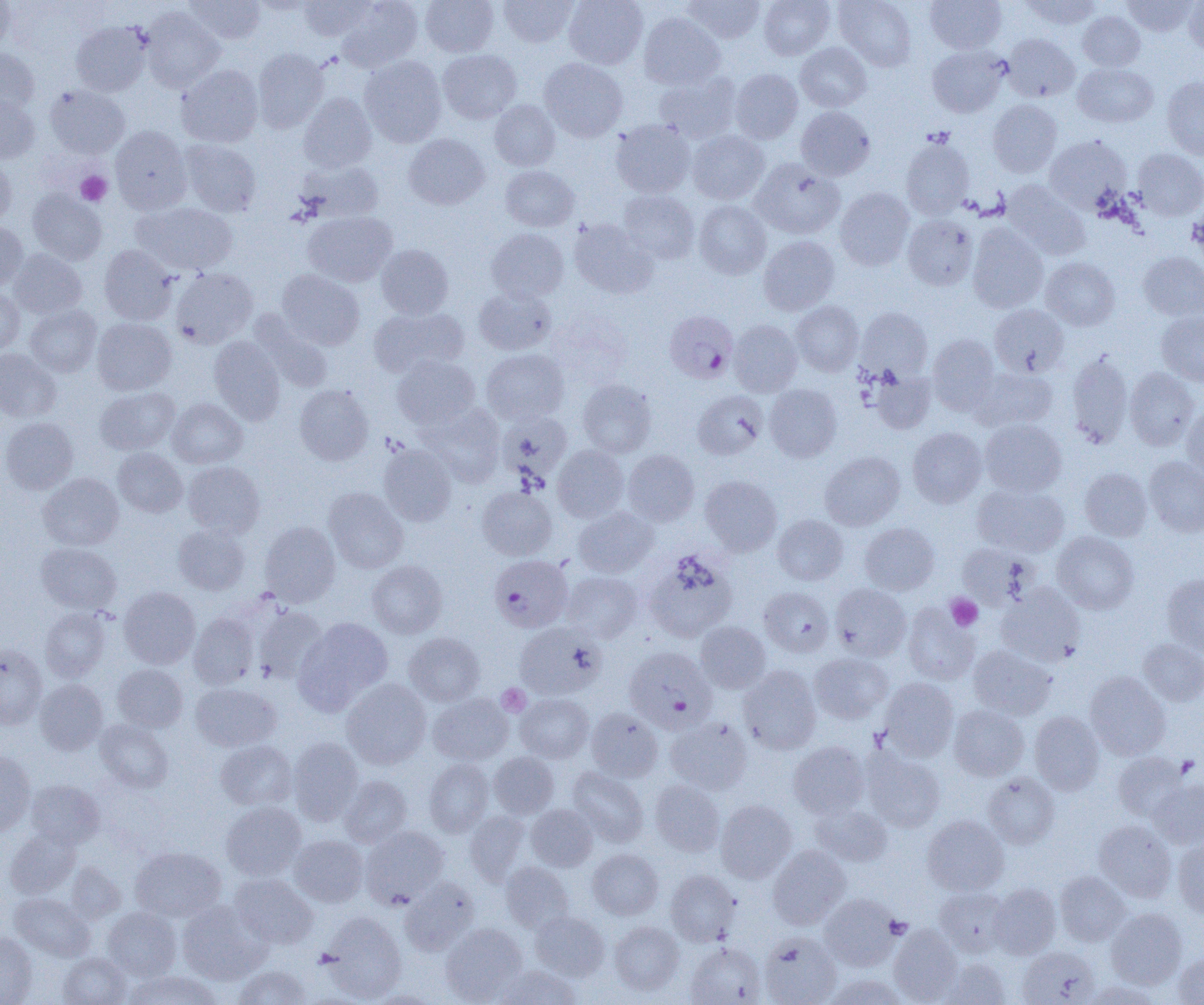
Summary:
  - Coordinate format: approximate bounding boxes as (x1, y1, x2, y2) in pixels
  - Uninfected red blood cell locations: (0, 0, 15, 54), (184, 0, 265, 45), (298, 0, 375, 40), (336, 0, 423, 72), (420, 0, 498, 57), (499, 0, 577, 47), (563, 0, 648, 69), (683, 0, 765, 45), (759, 0, 834, 60), (835, 0, 916, 71), (926, 0, 1006, 54), (1019, 0, 1102, 30), (1121, 0, 1199, 37), (1183, 0, 1204, 55), (142, 8, 225, 92), (1078, 11, 1145, 71), (639, 12, 725, 90), (71, 21, 151, 95), (1002, 34, 1079, 102), (794, 43, 872, 112), (927, 46, 1008, 117), (0, 48, 39, 113), (253, 48, 329, 134), (438, 49, 521, 124), (359, 56, 446, 147), (540, 58, 628, 142), (1072, 62, 1158, 128), (176, 65, 263, 147), (730, 68, 803, 144), (654, 72, 741, 144), (1161, 76, 1204, 159), (45, 84, 129, 158), (298, 92, 377, 172), (0, 94, 39, 163), (988, 99, 1062, 177), (489, 100, 560, 171), (795, 106, 875, 181), (610, 119, 695, 198), (109, 126, 192, 214), (688, 130, 769, 205), (404, 134, 490, 210), (1044, 135, 1131, 211), (901, 136, 974, 218), (179, 139, 261, 216), (1133, 149, 1204, 220), (0, 156, 16, 226), (750, 159, 845, 239), (297, 160, 384, 222), (500, 165, 580, 231), (1003, 181, 1090, 260), (835, 188, 914, 270), (27, 189, 107, 265), (619, 190, 699, 263), (693, 200, 771, 279), (132, 202, 237, 275), (303, 211, 397, 287), (902, 214, 978, 290), (568, 219, 658, 299), (0, 222, 28, 290), (967, 224, 1048, 313), (486, 228, 569, 302), (759, 235, 839, 315), (376, 244, 453, 319), (100, 245, 179, 325), (8, 249, 87, 319), (1138, 252, 1204, 322), (1041, 257, 1120, 330), (171, 268, 258, 349), (276, 269, 364, 350), (474, 286, 556, 355), (0, 287, 24, 355), (790, 301, 863, 376), (25, 304, 102, 377), (989, 304, 1069, 377), (369, 306, 469, 378), (855, 307, 933, 380), (251, 312, 333, 393), (1157, 312, 1204, 386), (92, 318, 176, 395), (728, 320, 802, 397), (927, 333, 999, 415), (209, 336, 285, 425), (0, 348, 61, 422), (481, 349, 569, 424), (1065, 350, 1133, 449), (392, 355, 480, 429), (971, 367, 1058, 431), (1125, 367, 1200, 451), (870, 369, 936, 434), (577, 379, 657, 458), (765, 384, 842, 462), (294, 385, 374, 466), (95, 387, 180, 455), (693, 391, 768, 460), (168, 398, 247, 468), (420, 403, 505, 487), (1182, 403, 1204, 481), (498, 412, 573, 485), (0, 417, 78, 494), (979, 419, 1066, 497), (907, 427, 987, 508), (378, 443, 457, 526), (552, 445, 629, 522), (113, 448, 187, 517), (623, 450, 699, 526), (820, 452, 905, 530), (1144, 455, 1204, 537), (183, 461, 265, 538), (1079, 467, 1152, 541), (39, 473, 124, 550), (700, 475, 782, 556), (972, 482, 1069, 556), (477, 486, 557, 560), (323, 487, 408, 573), (573, 506, 658, 577), (772, 514, 848, 585), (259, 521, 340, 607), (860, 522, 939, 595), (173, 524, 250, 595), (1052, 531, 1139, 614), (36, 542, 122, 614), (956, 542, 1035, 610), (645, 549, 737, 642), (367, 560, 447, 638), (562, 571, 642, 643), (1161, 573, 1204, 655), (831, 584, 911, 661), (996, 584, 1086, 667), (119, 587, 200, 669), (759, 587, 834, 657), (902, 602, 980, 685), (253, 605, 327, 683), (40, 607, 111, 682), (188, 614, 258, 689), (295, 617, 393, 713), (695, 621, 770, 693), (514, 622, 605, 699), (404, 632, 485, 706), (1138, 638, 1204, 706), (0, 643, 47, 728), (968, 645, 1057, 720), (809, 652, 892, 724), (113, 664, 188, 732), (739, 665, 822, 755), (1085, 671, 1171, 760), (341, 678, 431, 769), (878, 678, 959, 761), (35, 679, 108, 754), (191, 682, 281, 751), (428, 693, 512, 765), (515, 693, 594, 762), (948, 705, 1029, 780), (586, 707, 663, 781), (1029, 711, 1105, 794), (665, 717, 753, 795), (95, 720, 173, 793), (288, 737, 363, 824), (215, 739, 297, 811), (788, 741, 869, 818), (861, 747, 945, 832), (0, 751, 36, 836), (1112, 751, 1189, 821), (489, 752, 559, 818), (424, 758, 494, 837), (567, 767, 648, 847), (983, 772, 1059, 848), (339, 775, 412, 847), (1149, 779, 1204, 849), (26, 780, 104, 849), (649, 780, 725, 856), (716, 800, 797, 883), (221, 802, 306, 880), (810, 802, 893, 867), (526, 804, 598, 871), (464, 811, 531, 886), (922, 814, 1009, 896), (1094, 819, 1176, 902), (360, 826, 448, 908), (4, 828, 80, 899), (289, 835, 368, 907), (1172, 840, 1204, 918), (768, 845, 851, 929), (131, 846, 226, 923), (587, 849, 663, 920), (500, 861, 574, 932), (65, 863, 125, 924), (665, 870, 741, 946), (1055, 871, 1131, 946), (230, 873, 318, 949), (400, 877, 479, 955), (989, 883, 1061, 959), (935, 887, 1010, 957), (10, 893, 95, 961), (819, 893, 902, 970), (177, 900, 268, 984), (102, 907, 181, 980), (1106, 908, 1187, 989), (530, 910, 610, 981), (320, 913, 406, 1002), (609, 921, 684, 995), (441, 923, 527, 1003), (889, 925, 963, 1004), (0, 932, 38, 1004), (759, 932, 841, 1005), (686, 941, 765, 1004), (1018, 945, 1100, 1004), (1172, 952, 1204, 1004), (58, 953, 132, 1004), (939, 958, 1011, 1004), (232, 965, 312, 1005), (494, 965, 581, 1004), (125, 971, 222, 1005), (824, 974, 908, 1005), (1082, 981, 1163, 1005), (366, 991, 443, 1004)
  - Plasmodium falciparum-infected red blood cell locations: (664, 310, 738, 383), (489, 554, 573, 632), (625, 645, 717, 734)
  - Platelet locations: (75, 171, 112, 206), (945, 594, 982, 631), (497, 684, 531, 717), (1175, 755, 1200, 777)
  - Slide-level diagnosis: Plasmodium falciparum
  - Field of view: one of a larger specimen
  - Magnification: 1000x
  - Image size: 1204×1005 pixels
  - Modality: optical microscopy
  - Preparation: thin blood smear